Assess this cell for malaria.
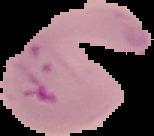
It is parasitized.

preparation = thin blood film
image type = cell region segmented out of the field of view; surrounding area masked to black
image size = 154×136 pixels